Classify this cell by malaria status.
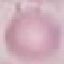
It is uninfected.

Summary:
  - Preparation: thin blood smear
  - Capture: smartphone camera at the microscope eyepiece
  - Image type: cell patch, automatically extracted from a larger field of view and resized to 64 × 64 pixels
  - Stain: Giemsa